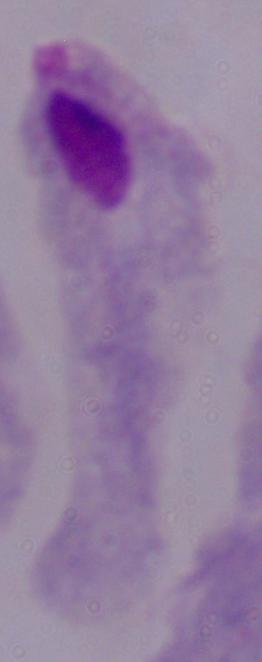
magnification = 1000x
identification = trichomonad
modality = photomicrograph